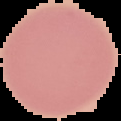

image size = 121×121 pixels
preparation = thin blood film
malaria status = uninfected
image type = cell region segmented out of the field of view; surrounding area masked to black